Outline platelets.
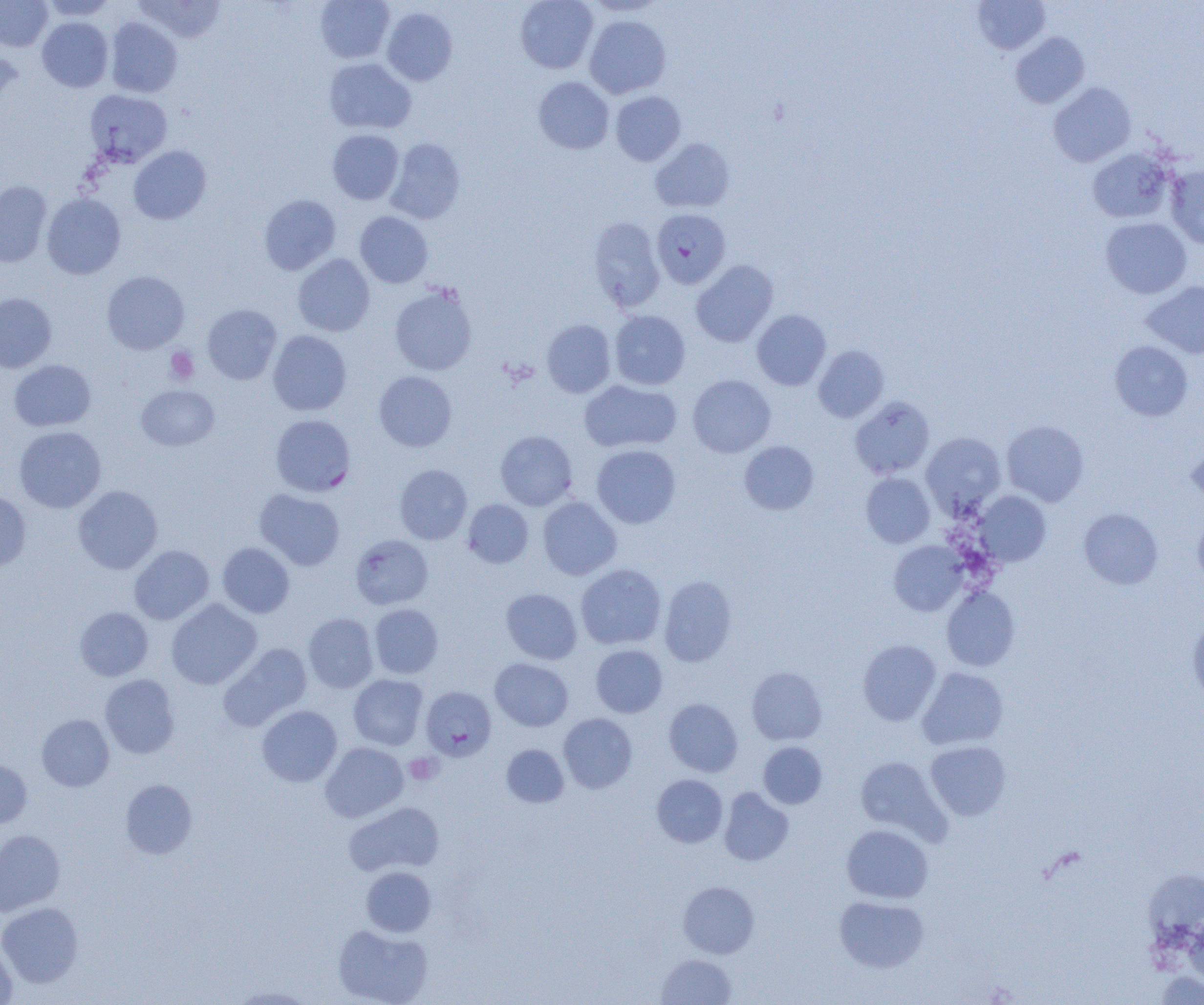
Approximate bounding boxes as (x1,y1)-(x2,y2) corner pairs in pixels.
Platelets: (165,348)-(199,385), (405,753)-(442,785).

Summary:
  - Uninfected red blood cell locations: (0,0)-(52,51), (40,0)-(118,20), (135,0)-(225,44), (315,0)-(394,63), (515,0)-(598,74), (972,0)-(1051,54), (381,7)-(457,86), (584,15)-(671,98), (37,17)-(113,92), (106,18)-(183,97), (1010,32)-(1089,109), (0,45)-(22,114), (324,58)-(417,134), (533,77)-(614,154), (1048,82)-(1136,167), (610,91)-(686,165), (327,129)-(404,204), (385,137)-(465,224), (651,137)-(734,213), (128,145)-(212,225), (1087,148)-(1176,224), (1166,165)-(1204,249), (0,180)-(52,268), (42,193)-(126,279), (259,194)-(341,275), (355,211)-(433,288), (587,217)-(665,312), (1100,217)-(1192,299), (293,254)-(375,336), (691,260)-(778,347), (102,270)-(189,354), (1141,281)-(1204,358), (389,283)-(478,375), (0,293)-(57,373), (202,304)-(282,384), (751,309)-(831,390), (610,310)-(690,389), (541,319)-(616,397), (267,330)-(352,415), (1110,341)-(1193,421), (814,345)-(889,422), (9,360)-(96,432), (374,371)-(457,452), (687,374)-(776,457), (579,379)-(681,453), (137,384)-(219,451), (850,396)-(935,479), (1001,420)-(1089,506), (14,426)-(106,512), (495,430)-(577,510), (921,432)-(1005,516), (1186,438)-(1204,505), (739,441)-(818,515), (591,444)-(681,528), (394,464)-(472,544), (861,472)-(935,548), (73,485)-(162,574), (255,489)-(345,570), (0,490)-(32,570), (975,491)-(1051,566), (537,497)-(622,580), (462,499)-(533,568), (1079,508)-(1163,589), (1192,514)-(1204,587), (889,541)-(968,616), (217,542)-(295,618), (129,545)-(214,624), (576,564)-(666,650), (659,575)-(737,667), (941,586)-(1020,671), (501,588)-(582,664), (166,599)-(262,689), (369,603)-(443,678), (74,606)-(153,681), (303,613)-(378,693), (1187,616)-(1204,705), (858,640)-(941,726), (219,643)-(312,731), (590,644)-(667,717), (490,658)-(573,731), (747,666)-(827,745), (917,667)-(1009,750), (100,674)-(180,758), (349,674)-(428,750), (664,698)-(743,776), (257,705)-(342,786), (558,713)-(637,793), (36,714)-(114,791), (925,740)-(1012,820), (320,742)-(408,822), (758,742)-(827,808), (501,744)-(569,807), (855,756)-(949,842), (0,760)-(32,830), (651,774)-(727,848), (120,779)-(197,858), (719,787)-(794,866), (344,802)-(445,876), (841,824)-(933,904), (0,829)-(65,916), (362,866)-(436,936), (1143,870)-(1204,943), (679,881)-(759,958), (834,895)-(928,972), (0,902)-(83,987), (1184,915)-(1204,987), (333,924)-(433,1005), (0,939)-(17,1004), (656,954)-(737,1004), (1157,972)-(1204,1005), (229,986)-(315,1004)
  - Plasmodium falciparum-infected red blood cell locations: (85,90)-(172,167), (651,209)-(731,288), (270,414)-(355,496), (351,534)-(433,609), (422,686)-(496,761)
  - Slide-level diagnosis: Plasmodium falciparum
  - Field of view: one of a larger specimen
  - Magnification: 1000x
  - Preparation: thin blood smear
  - Modality: light microscopy
  - Image size: 1204×1005 pixels